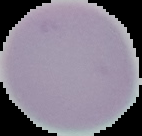

Summary:
  - Preparation: thin blood film
  - Image size: 142×136 pixels
  - Result: no Plasmodium parasites detected
  - Image type: segmented cell region on a black background